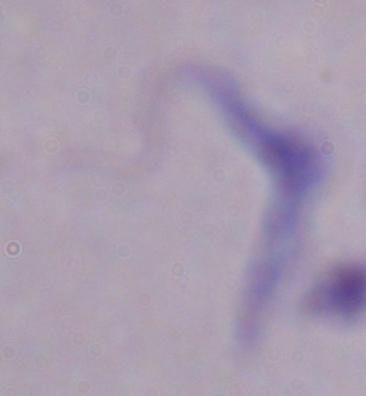
magnification: 1000x
modality: photomicrograph
identification: trypanosome